Point out each leukocyte.
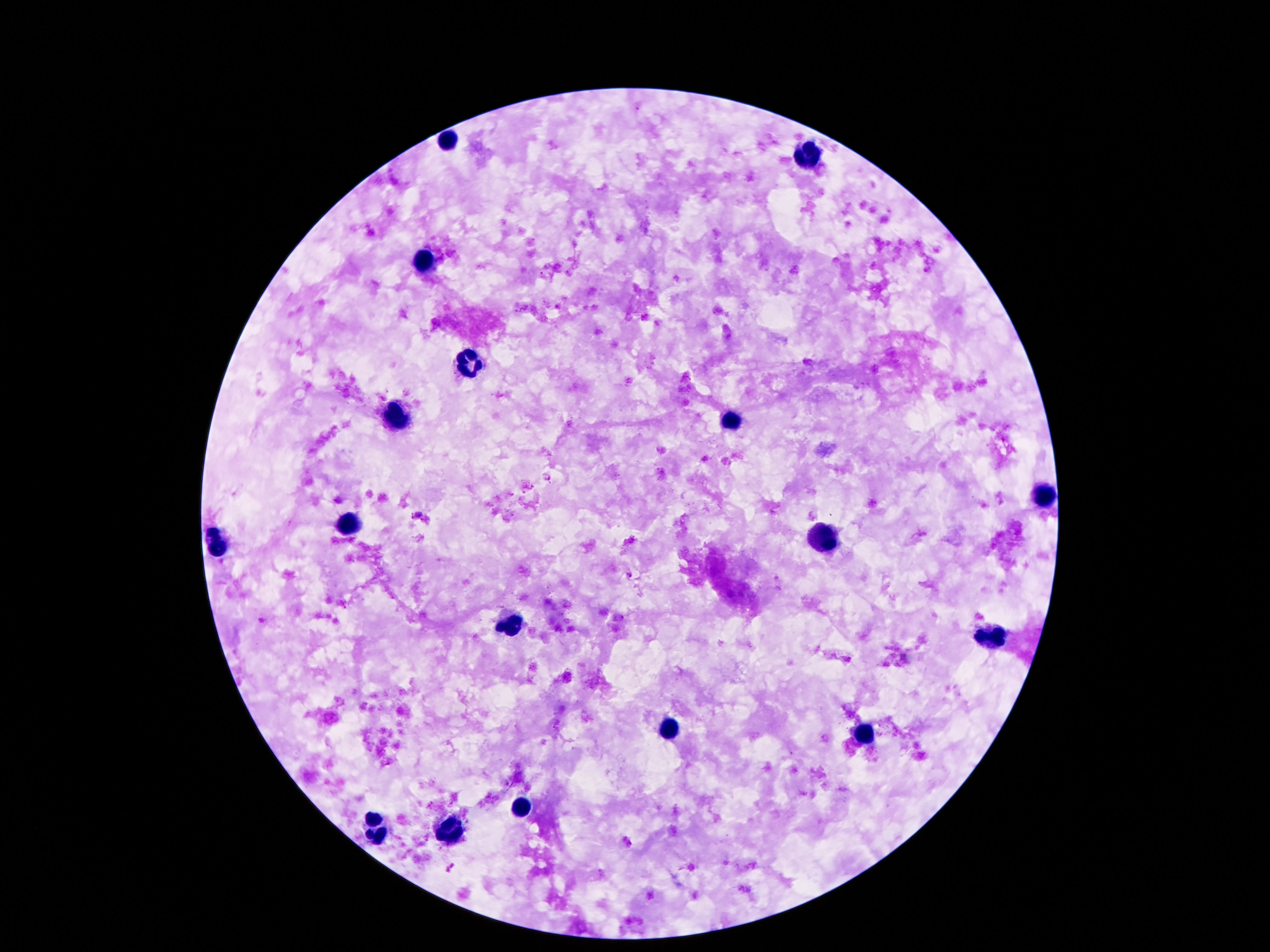

Approximate centers as {x, y} in pixels.
Leukocytes: {448, 142}, {807, 156}, {423, 265}, {471, 362}, {397, 414}, {731, 424}, {1040, 496}, {349, 523}, {822, 538}, {215, 546}, {511, 625}, {990, 636}, {862, 732}, {672, 733}, {521, 808}, {376, 831}, {448, 835}.

Summary:
  - Image size: 1270×952 pixels
  - Capture: smartphone camera through the microscope eyepiece
  - Stain: Giemsa
  - Field of view: single
  - Magnification: 100x
  - Preparation: thick blood smear
  - Patient malaria status: negative